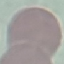

Summary:
  - Result: negative for malaria parasites
  - Capture: smartphone through the microscope eyepiece
  - Stain: Giemsa
  - Preparation: thin smear
  - Image type: cell patch, automatically extracted from a larger field of view and resized to 64 × 64 pixels